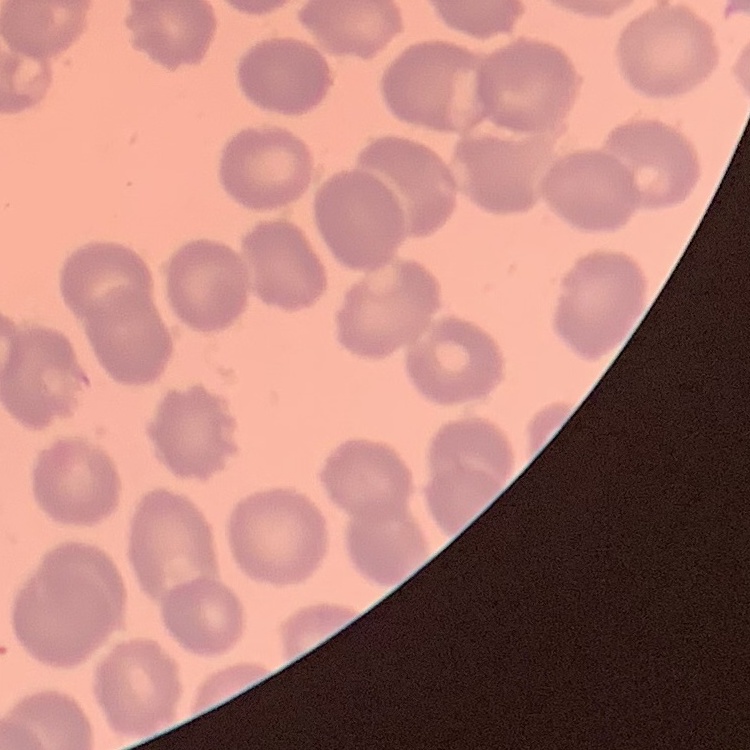
red blood cell morphology = no rouleaux formation
preparation = thin blood smear
image type = square crop of a larger photomicrograph
stain = Field's or Giemsa